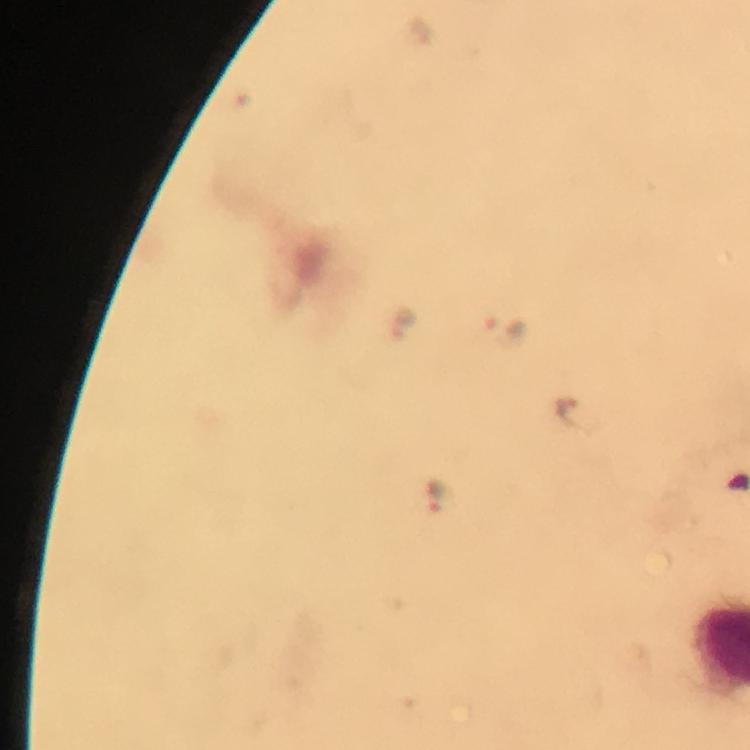
Approximate centers as [x, y] in pixels.
Summary:
  - Malaria parasite locations: [402, 320], [503, 328], [572, 413], [436, 494]
  - Image size: 750×750 pixels
  - Immersion oil: used
  - Preparation: thick blood smear
  - Magnification: 100x
  - Context: from a diagnostic examination for malaria
  - Stain: Giemsa
  - Capture: smartphone photograph through a microscope
  - Cropped from: one field of view